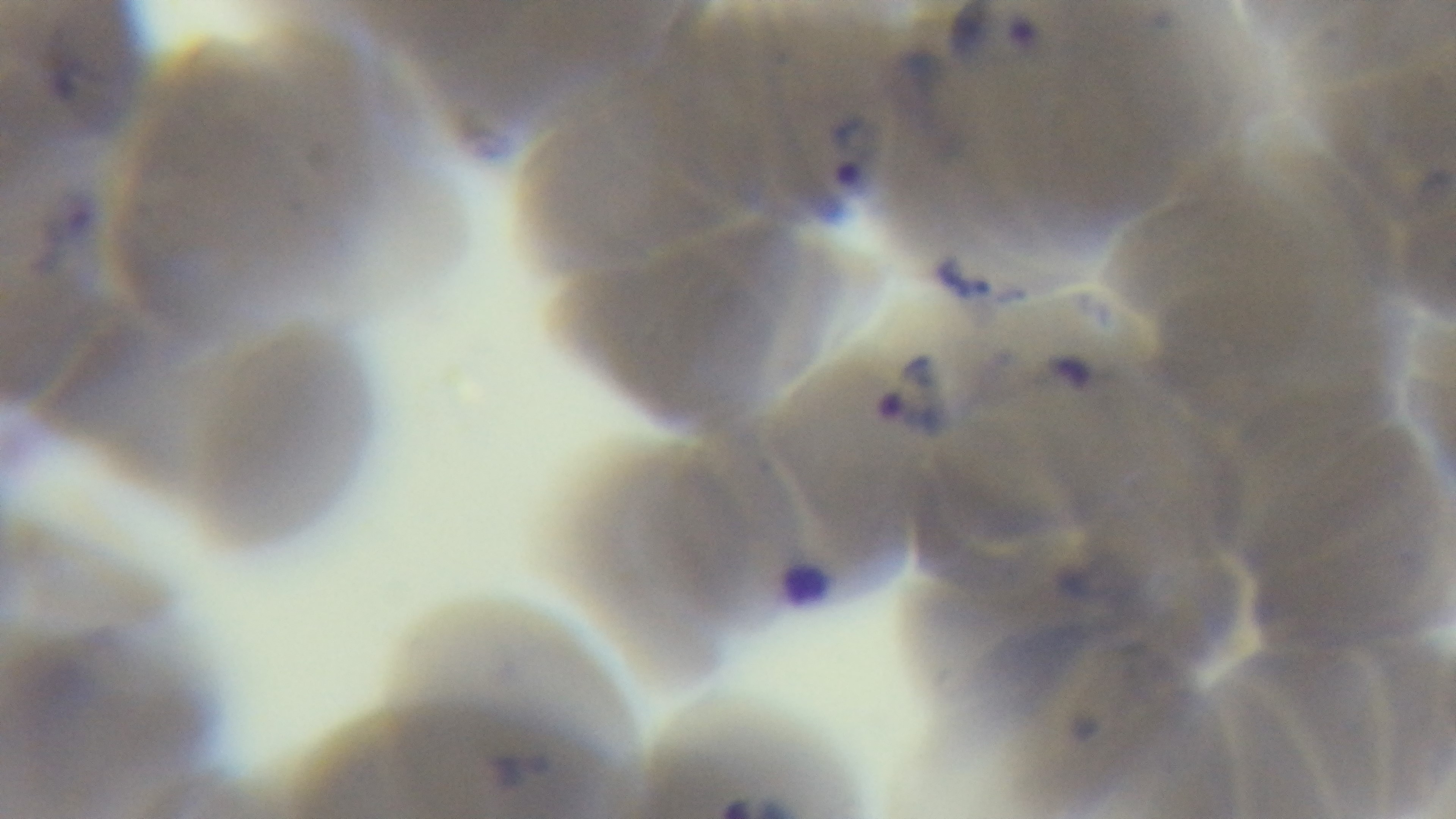
{
  "stain": "Giemsa",
  "objective": "100x oil immersion",
  "modality": "light microscopy",
  "capture": "mounted 4K digital camera",
  "malaria_status": "infected",
  "field_of_view": "single",
  "preparation": "thin blood film"
}